Classify this cell by malaria status.
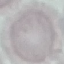

It is uninfected.

stain: Giemsa
preparation: thin smear
image_type: cell patch, automatically extracted from a larger field of view and resized to 64 × 64 pixels
capture: smartphone through the microscope eyepiece